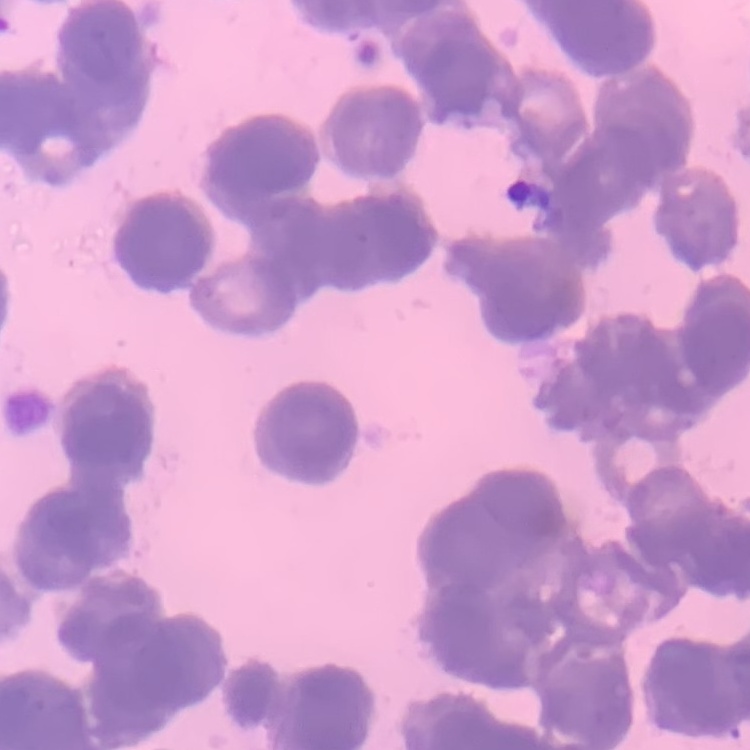

Summary:
  - Red blood cell morphology: rouleaux formation
  - Stain: Field's or Giemsa
  - Preparation: thin blood smear
  - Image type: square crop of a larger photomicrograph